Report the malaria status of this cell.
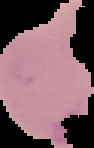
Uninfected.

Summary:
  - Image type: segmented cell region with the area outside set to black
  - Preparation: thin blood film
  - Image size: 94×148 pixels